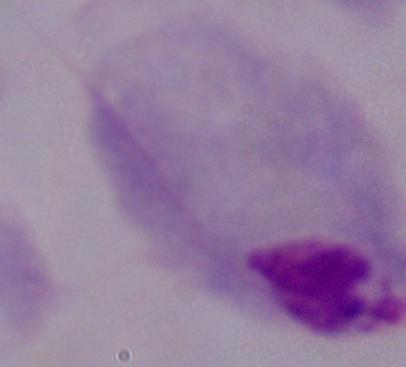 A trichomonad is seen. 1000x magnification. Photomicrograph.